Assess for parasitized red blood cells.
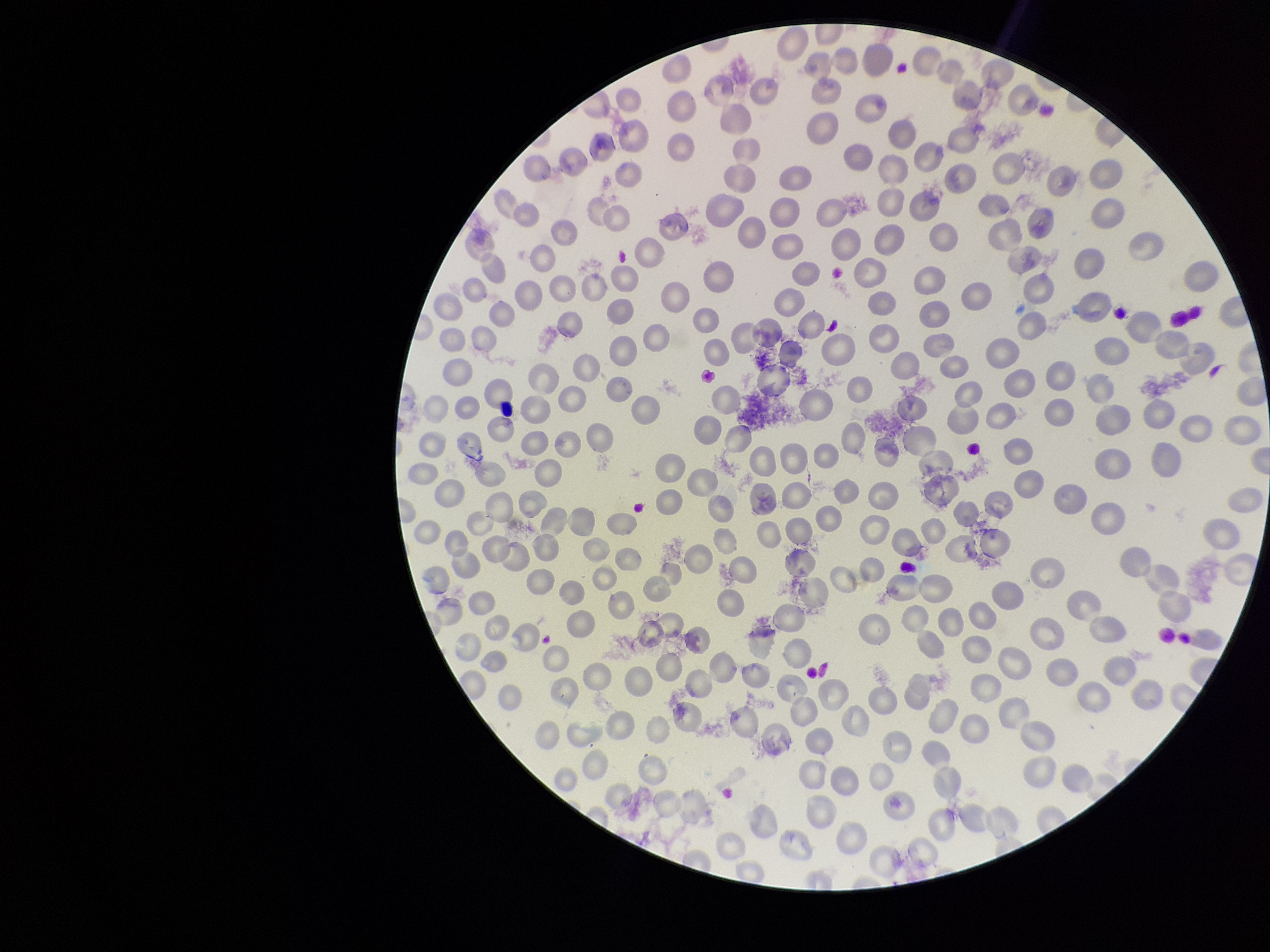

None seen.

Summary:
  - Patient malaria status: positive
  - Species reported for this patient: Plasmodium vivax
  - Field of view: single
  - Capture: smartphone photograph through the microscope eyepiece
  - Red blood cell count: 249
  - Preparation: thin
  - Parasitized red blood cell count: 0
  - Image size: 1270×952 pixels
  - Stain: Giemsa